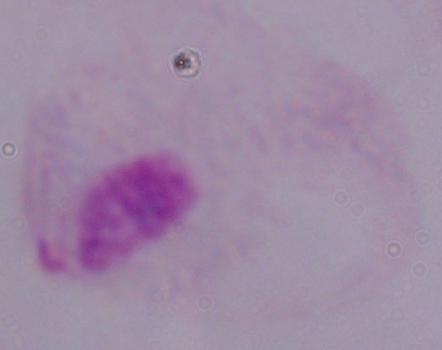
Micrograph. A trichomonad is shown. 1000x magnification.